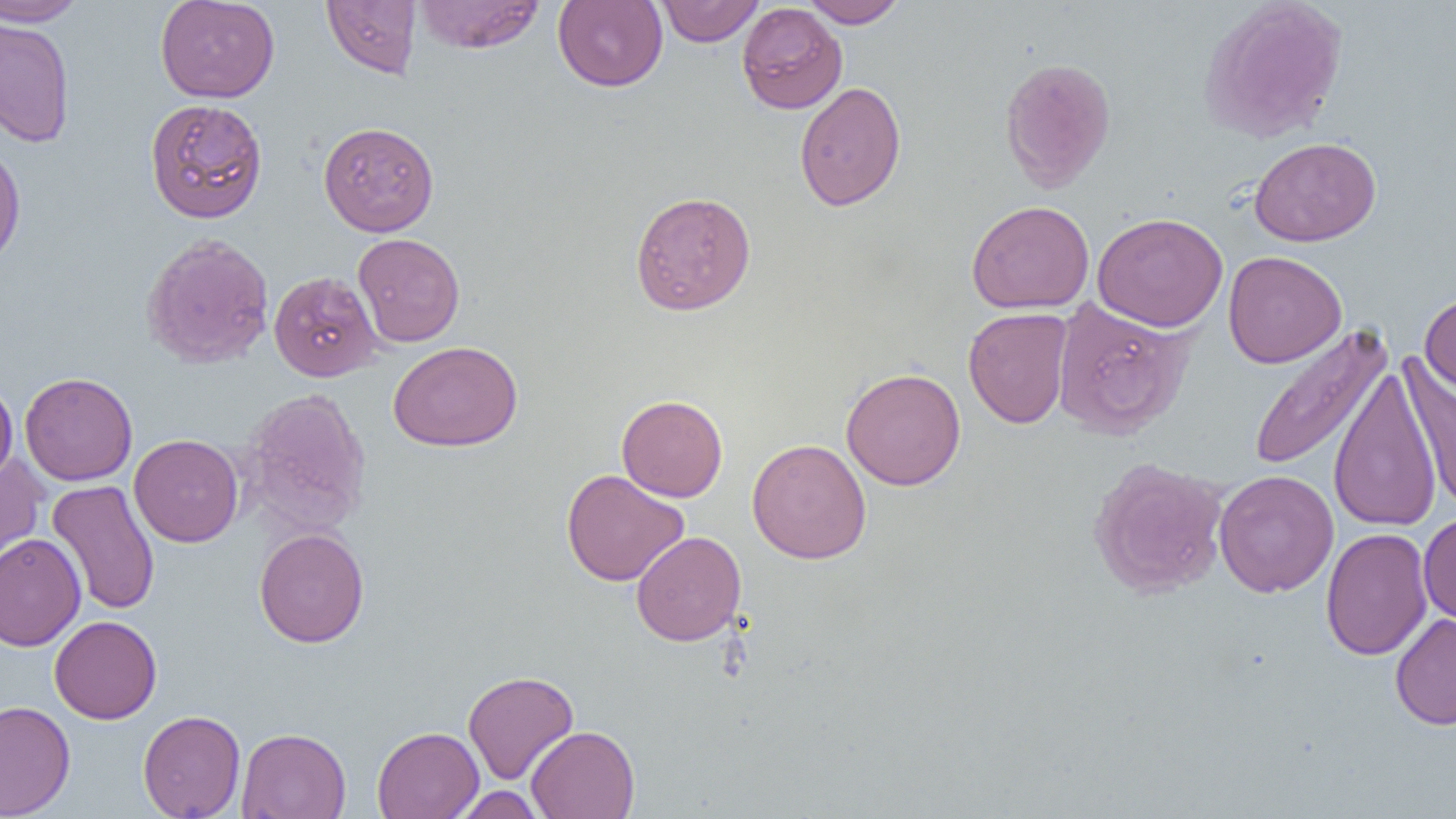

slide-level diagnosis = no evidence of blood parasites
preparation = thin blood smear
modality = light microscopy
image size = 1456×819 pixels
magnification = 1000x
uninfected red blood cell locations = approximate bounding boxes as (x1,y1)-(x2,y2) corner pairs in pixels: (0,0)-(88,26), (155,0)-(279,103), (321,0)-(421,79), (412,0)-(546,54), (553,0)-(667,91), (656,0)-(764,47), (801,0)-(906,28), (1199,0)-(1349,143), (736,3)-(848,114), (0,17)-(76,148), (999,56)-(1116,192), (794,81)-(906,212), (144,98)-(268,223), (318,121)-(439,237), (1249,136)-(1381,246), (0,144)-(26,270), (630,190)-(756,316), (967,200)-(1094,314), (1092,212)-(1228,332), (141,232)-(275,369), (352,232)-(465,347), (1223,250)-(1347,368), (269,270)-(382,382), (1419,291)-(1456,396), (1051,298)-(1195,440), (963,307)-(1072,428), (1244,324)-(1392,474), (388,340)-(522,451), (1397,357)-(1456,511), (1328,366)-(1444,533), (841,367)-(966,490), (19,372)-(138,486), (0,379)-(18,486), (241,387)-(372,535), (616,394)-(728,502), (129,433)-(244,547), (747,438)-(871,563), (0,453)-(49,576), (1087,456)-(1229,598), (560,468)-(689,587), (1214,469)-(1339,598), (46,480)-(160,615), (1418,513)-(1456,626), (1320,527)-(1433,661), (254,528)-(369,648), (631,531)-(747,646), (0,532)-(86,652), (1390,612)-(1456,730), (50,616)-(161,724), (463,670)-(579,784), (0,700)-(75,818), (138,710)-(245,819), (526,725)-(640,819), (372,726)-(484,819), (237,727)-(351,819), (451,786)-(545,818)
field of view = single